Name the blood parasite species.
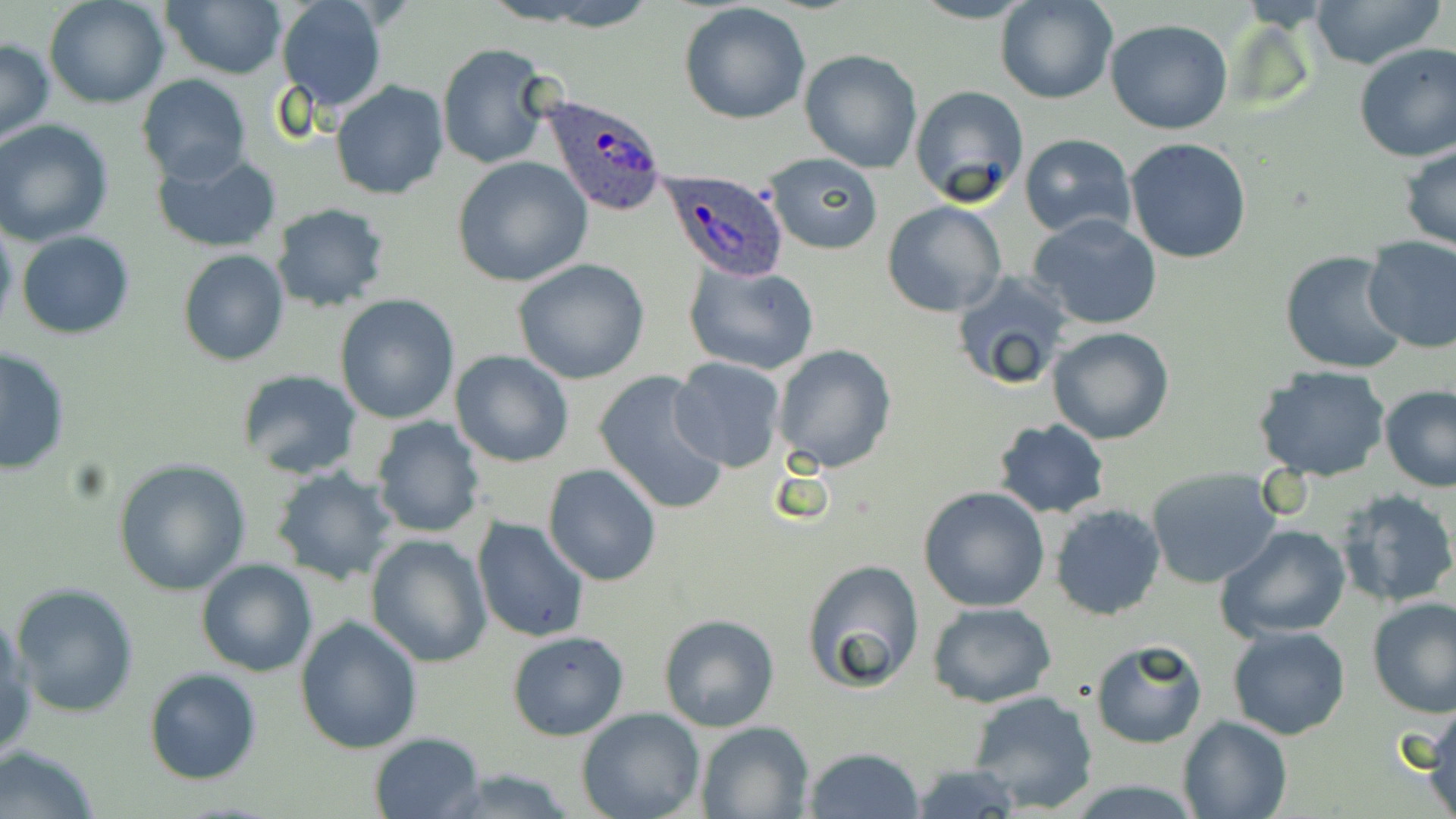
Plasmodium ovale.

magnification: 1000x
plasmodium_ovale_infected_red_blood_cell_locations: 'approximate bounding boxes as (x1, y1, x2, y2) in pixels: (539, 93, 670, 216), (655, 168, 791, 278)'
field_of_view: single
image_size: 1456×819 pixels
stain: May-Grünwald-Giemsa
modality: light microscopy
preparation: thin blood film
uninfected_red_blood_cell_locations: 'approximate bounding boxes as (x1, y1, x2, y2) in pixels: (43, 0, 170, 108), (491, 0, 664, 30), (994, 0, 1118, 105), (1305, 0, 1448, 69), (161, 1, 287, 80), (275, 1, 389, 114), (679, 2, 812, 126), (1105, 19, 1235, 134), (0, 38, 54, 144), (1352, 42, 1456, 163), (437, 45, 560, 171), (798, 48, 923, 174), (135, 75, 252, 186), (331, 80, 450, 201), (909, 85, 1030, 208), (1, 119, 117, 246), (1018, 134, 1137, 239), (1124, 137, 1254, 265), (1401, 144, 1456, 251), (152, 150, 283, 253), (763, 153, 884, 256), (452, 156, 593, 287), (881, 201, 1007, 317), (271, 203, 391, 314), (1027, 213, 1165, 331), (0, 215, 18, 341), (16, 230, 135, 339), (1362, 235, 1456, 353), (178, 249, 289, 365), (1280, 253, 1410, 376), (511, 258, 651, 385), (684, 262, 820, 377), (948, 270, 1074, 392), (334, 294, 460, 425), (1046, 326, 1176, 444), (0, 343, 71, 474), (769, 343, 897, 473), (449, 348, 575, 469), (669, 357, 786, 474), (1254, 364, 1392, 482), (592, 369, 732, 515), (235, 371, 365, 479), (1379, 384, 1456, 492), (368, 417, 487, 538), (989, 419, 1111, 519), (114, 458, 253, 596), (542, 463, 664, 585), (271, 466, 402, 586), (1143, 466, 1282, 588), (917, 485, 1051, 612), (1333, 488, 1455, 610), (1049, 502, 1167, 621), (472, 517, 592, 644), (1216, 526, 1351, 641), (365, 534, 491, 667), (196, 558, 317, 676), (799, 558, 927, 695), (10, 582, 140, 718), (1366, 597, 1456, 716), (927, 601, 1057, 708), (0, 613, 34, 763), (658, 613, 781, 733), (295, 617, 423, 756), (1227, 625, 1352, 741), (507, 630, 629, 741), (1089, 639, 1209, 749), (144, 668, 264, 785), (968, 690, 1099, 814), (1426, 704, 1456, 817), (577, 707, 706, 819), (1176, 715, 1292, 819), (696, 720, 815, 818), (368, 732, 487, 819), (0, 743, 102, 819), (802, 746, 923, 819), (907, 762, 1024, 819), (433, 768, 585, 819)'